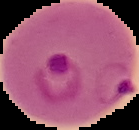
From a thin blood smear. The area outside the segmented cell region is set to black. Malaria status: parasitized. Image is 139×130 pixels.